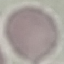
Summary:
  - Malaria status: uninfected
  - Image type: automatically extracted cell patch, resized to 64 × 64 pixels
  - Capture: smartphone through the microscope eyepiece
  - Preparation: thin smear
  - Stain: Giemsa